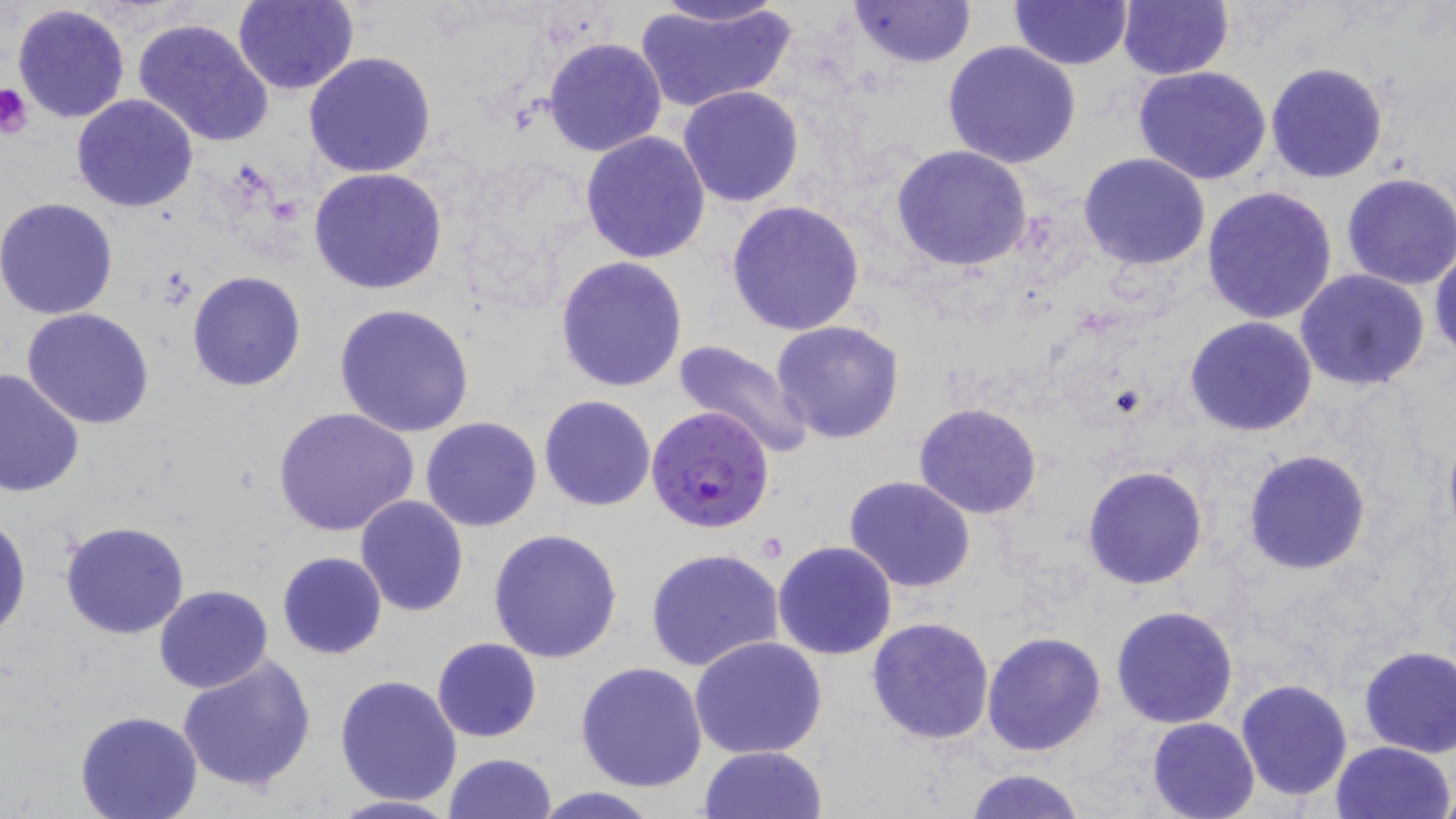
Summary:
  - Coordinate format: approximate bounding boxes as (x1,y1)-(x2,y2) corner pairs in pixels
  - Platelet locations: (0,82)-(32,138)
  - Uninfected red blood cell locations: (231,0)-(359,95), (641,0)-(794,29), (849,0)-(975,69), (1118,0)-(1233,80), (1011,1)-(1134,70), (635,2)-(797,111), (11,5)-(131,124), (132,17)-(275,148), (543,37)-(667,158), (942,41)-(1082,170), (304,50)-(438,178), (1265,61)-(1391,184), (1132,66)-(1275,186), (678,85)-(804,207), (70,94)-(199,213), (579,132)-(711,264), (891,145)-(1033,270), (1078,152)-(1211,272), (308,166)-(448,295), (1340,173)-(1456,291), (1200,186)-(1339,325), (0,197)-(120,319), (725,200)-(866,337), (1429,239)-(1456,367), (556,256)-(689,393), (1293,269)-(1431,391), (187,271)-(306,392), (332,302)-(476,436), (21,308)-(157,429), (1185,316)-(1318,438), (771,320)-(906,443), (670,340)-(816,462), (0,369)-(85,499), (538,395)-(655,511), (914,402)-(1042,518), (274,407)-(421,539), (421,416)-(543,532), (1241,449)-(1371,576), (1082,465)-(1209,590), (843,474)-(976,594), (354,495)-(470,618), (0,512)-(31,641), (60,520)-(190,640), (488,528)-(623,665), (771,541)-(897,660), (645,547)-(784,672), (277,551)-(387,659), (153,584)-(273,694), (1110,605)-(1239,729), (866,616)-(996,745), (981,632)-(1107,756), (688,635)-(828,759), (432,637)-(542,743), (1358,646)-(1456,758), (176,654)-(318,793), (576,660)-(708,792), (334,675)-(463,806), (1236,679)-(1353,802), (73,711)-(203,819), (1147,717)-(1260,819), (1329,740)-(1454,819), (698,746)-(828,819), (442,753)-(559,818), (964,767)-(1087,818), (527,788)-(667,818), (321,793)-(464,818)
  - Plasmodium falciparum-infected red blood cell locations: (646,405)-(775,534)
  - Slide-level diagnosis: Plasmodium falciparum
  - Magnification: 1000x
  - Modality: light microscopy
  - Preparation: thin blood smear
  - Stain: May-Grünwald-Giemsa
  - Image size: 1456×819 pixels
  - Field of view: single